Give the position of every leukocyte visible.
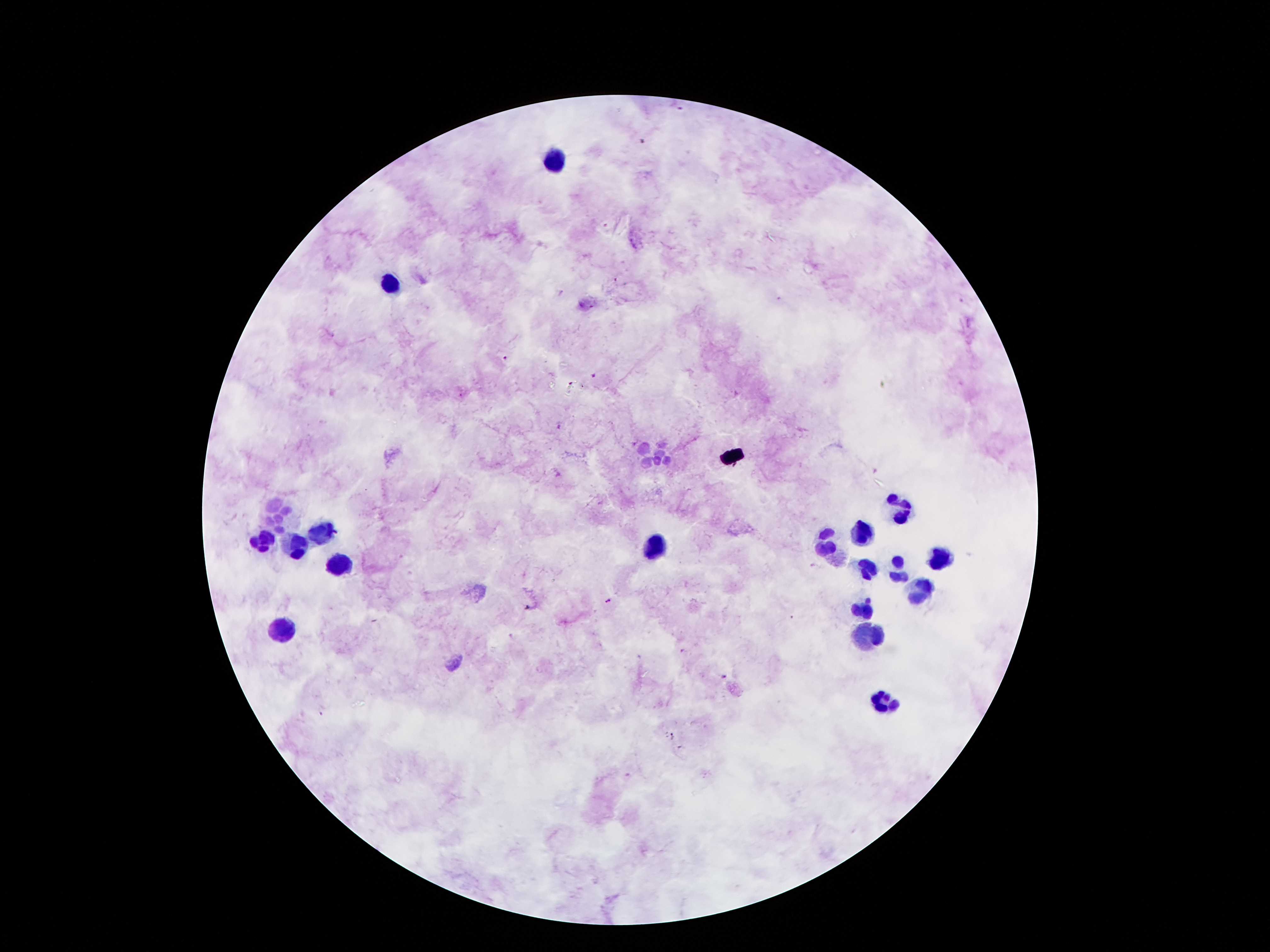
Approximate centers as [x, y] in pixels.
Leukocytes: [555, 161], [393, 282], [655, 455], [896, 509], [280, 513], [860, 534], [317, 536], [827, 542], [262, 543], [301, 546], [655, 549], [938, 560], [341, 566], [866, 572], [899, 572], [920, 591], [862, 608], [281, 629], [871, 632], [884, 702].

Malaria parasite locations: [642, 143], [504, 358], [592, 377], [571, 384], [559, 427], [633, 444], [608, 602], [682, 651], [725, 676], [321, 712], [672, 736]. Thick blood film. Patient malaria status: positive for Plasmodium falciparum. Single field of view. Smartphone photograph taken through the microscope eyepiece. Giemsa-stained preparation. Image is 1270×952 pixels. 100x magnification.